Give the position of every malaria parasite.
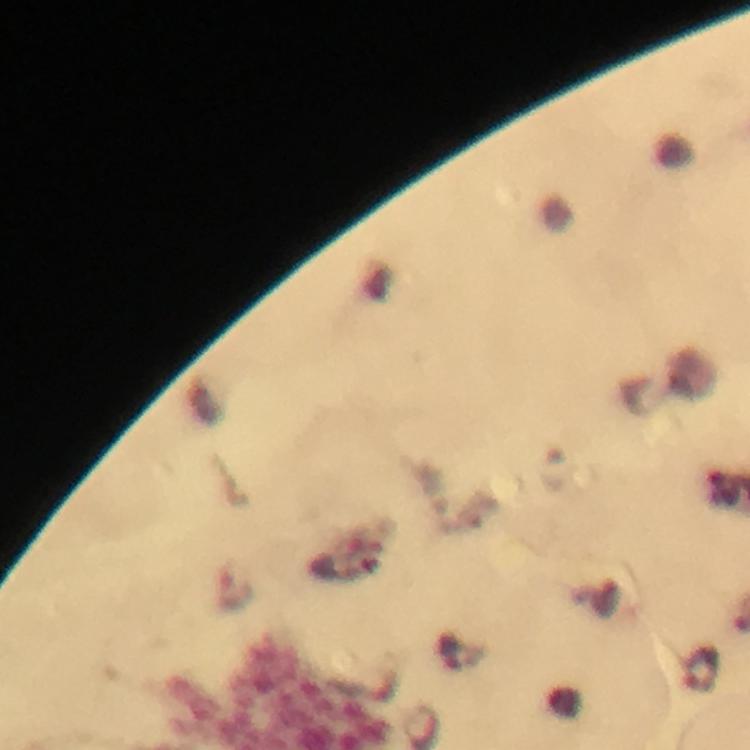
Approximate centers as {x, y} in pixels.
Malaria parasites: {698, 669}.

From a malaria diagnostic workup. Cropped region of a single field of view. Image is 750×750 pixels. Giemsa stain. Thick blood smear. Immersion oil was used. Photographed through the microscope with a smartphone camera. At 100x magnification.